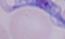
identification = trypanosome
modality = photomicrograph
magnification = 1000x